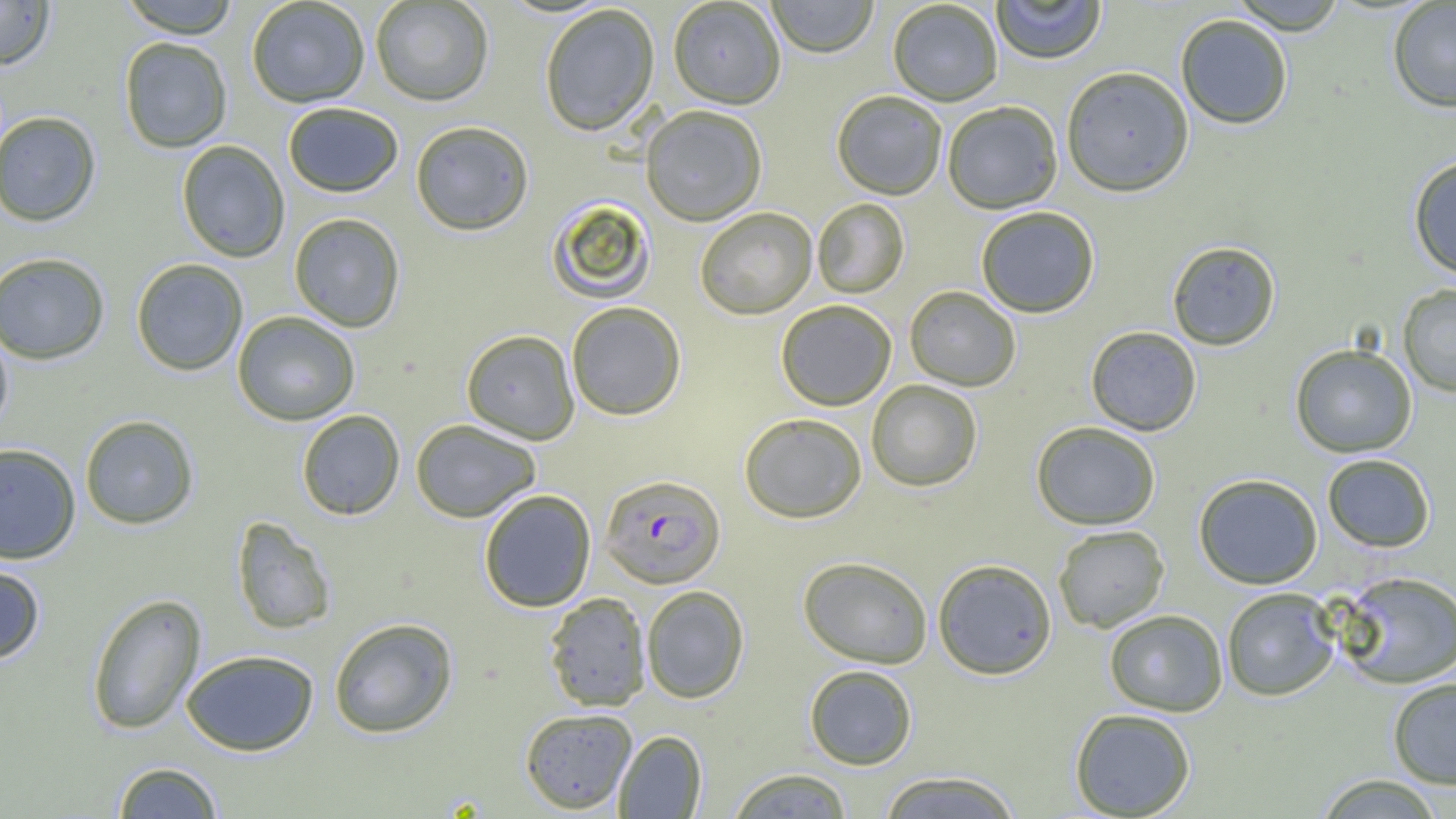
Approximate bounding boxes as [x1, y1, x2, y2] in pixels. Uninfected red blood cell locations: [0, 0, 55, 70], [118, 0, 241, 38], [246, 0, 370, 108], [767, 0, 878, 59], [991, 0, 1107, 65], [1228, 0, 1348, 35], [370, 1, 495, 107], [668, 1, 786, 110], [887, 1, 1003, 107], [1387, 1, 1456, 113], [539, 4, 659, 136], [1175, 15, 1294, 130], [119, 38, 233, 153], [1061, 67, 1194, 198], [831, 91, 947, 201], [943, 101, 1062, 214], [283, 102, 403, 197], [640, 106, 767, 226], [0, 111, 102, 227], [410, 120, 534, 236], [176, 140, 290, 263], [1408, 155, 1456, 280], [546, 198, 656, 304], [812, 198, 910, 299], [695, 207, 817, 320], [976, 207, 1100, 318], [288, 212, 406, 332], [1167, 241, 1281, 352], [0, 251, 111, 365], [130, 258, 249, 376], [1397, 284, 1456, 397], [904, 286, 1021, 391], [776, 300, 897, 411], [566, 302, 686, 421], [232, 311, 360, 426], [0, 325, 14, 436], [1085, 327, 1202, 436], [461, 329, 580, 444], [1290, 344, 1418, 457], [866, 381, 982, 492], [296, 410, 405, 520], [738, 412, 867, 524], [79, 414, 200, 530], [411, 420, 541, 522], [1032, 422, 1161, 530], [0, 443, 81, 564], [1322, 454, 1436, 552], [1193, 474, 1323, 590], [478, 489, 596, 612], [231, 516, 336, 635], [1053, 525, 1169, 633], [797, 556, 933, 669], [0, 559, 47, 665], [932, 559, 1057, 680], [1334, 571, 1456, 689], [641, 585, 750, 703], [1221, 588, 1340, 701], [543, 592, 652, 712], [86, 593, 207, 735], [1104, 609, 1228, 716], [329, 617, 458, 738], [180, 649, 320, 756], [804, 665, 917, 769], [1387, 678, 1456, 789], [519, 708, 637, 814], [1069, 708, 1196, 818], [614, 730, 707, 818], [111, 761, 224, 818], [725, 767, 854, 819], [876, 770, 1024, 818], [1313, 774, 1446, 818]. Plasmodium falciparum-infected red blood cell locations: [599, 474, 725, 589]. Slide-level diagnosis: Plasmodium falciparum. One field of a larger specimen. Image is 1456×819 pixels. Thin blood smear. Light microscopy. Captured at 1000x magnification.